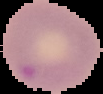

From a thin blood smear. Image is 103×94 pixels. The area outside the segmented cell region is set to black. Malaria status: parasitized.